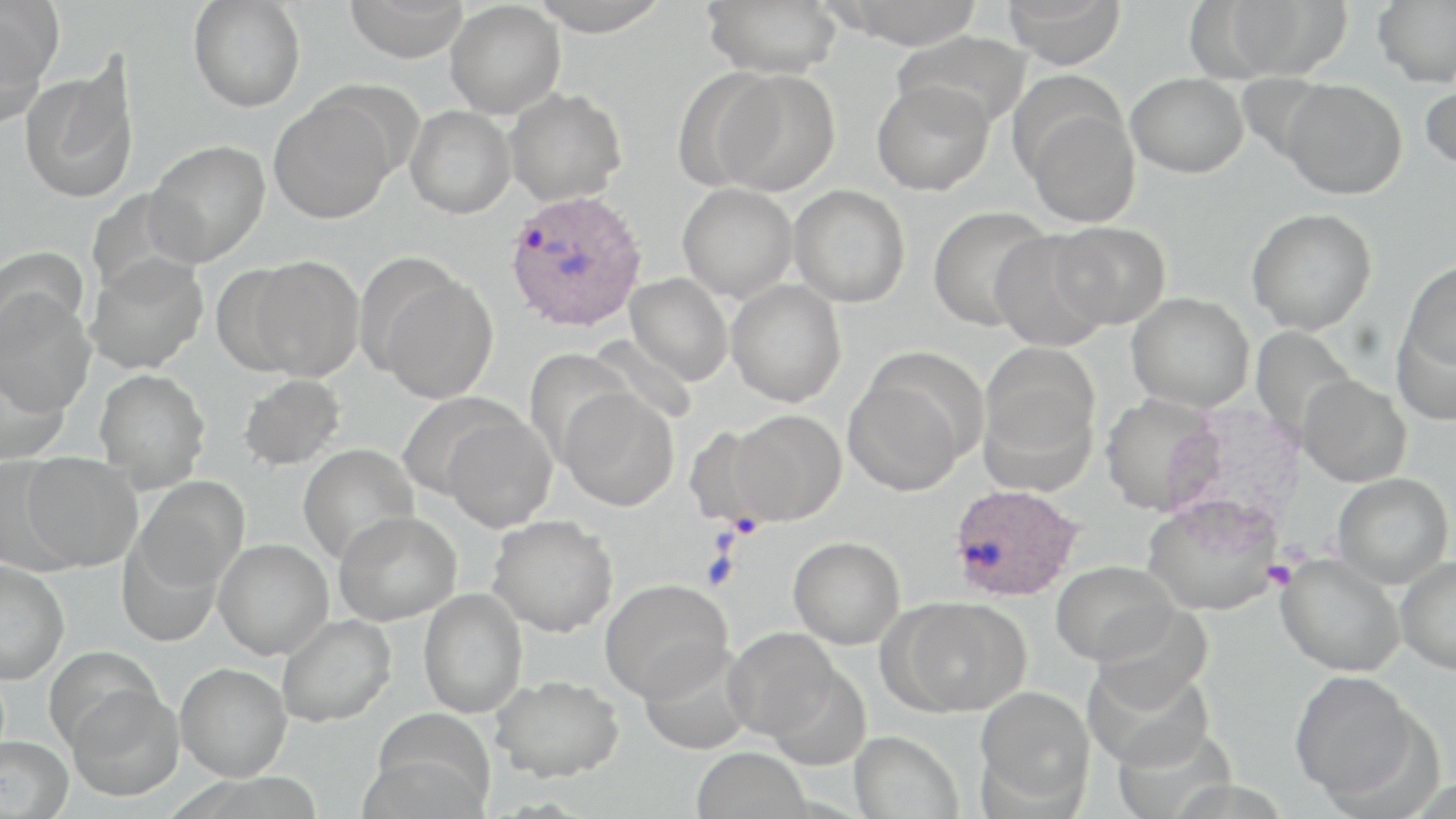
Plasmodium ovale-infected red blood cell locations = approximate bounding boxes as (x1,y1)-(x2,y2) corner pairs in pixels: (504,190)-(647,332), (948,483)-(1083,602)
slide-level diagnosis = Plasmodium ovale
field of view = one of a larger specimen
magnification = 1000x
uninfected red blood cell locations = approximate bounding boxes as (x1,y1)-(x2,y2) corner pairs in pixels: (344,0)-(471,63), (527,0)-(672,36), (831,0)-(986,50), (1001,0)-(1127,69), (1214,0)-(1351,80), (1373,0)-(1456,88), (188,1)-(306,113), (445,1)-(566,118), (701,1)-(844,78), (0,2)-(60,125), (892,29)-(1031,132), (19,65)-(139,203), (711,69)-(841,196), (1126,73)-(1248,177), (1279,78)-(1407,199), (1420,80)-(1456,174), (872,81)-(994,196), (504,88)-(627,206), (268,96)-(395,224), (1021,101)-(1141,228), (406,106)-(515,219), (145,140)-(270,266), (677,183)-(797,301), (788,184)-(910,308), (86,187)-(203,299), (927,205)-(1053,331), (1246,208)-(1377,335), (1051,221)-(1171,330), (990,230)-(1115,351), (0,247)-(88,343), (84,254)-(208,375), (242,255)-(365,381), (1399,260)-(1456,377), (373,270)-(498,404), (626,273)-(733,385), (726,280)-(847,407), (0,289)-(97,417), (1126,292)-(1254,413), (1392,309)-(1456,426), (978,341)-(1100,481), (524,347)-(636,464), (0,356)-(72,463), (94,368)-(211,492), (843,369)-(970,496), (238,374)-(346,471), (1297,374)-(1411,487), (559,388)-(679,511), (1100,393)-(1223,516), (727,409)-(846,525), (440,412)-(556,531), (298,444)-(419,564), (21,453)-(142,571), (0,455)-(80,574), (1332,472)-(1453,588), (133,475)-(250,592), (1142,494)-(1284,616), (334,510)-(462,625), (487,514)-(618,637), (116,536)-(225,645), (788,536)-(905,649), (213,538)-(333,659), (1276,553)-(1405,677), (1395,556)-(1456,675), (1051,559)-(1177,665), (0,560)-(70,683), (600,578)-(732,702), (419,588)-(528,718), (888,596)-(1032,716), (276,614)-(396,727), (723,627)-(841,742), (637,643)-(753,756), (44,645)-(162,751), (1084,658)-(1212,770), (175,662)-(292,781), (1289,667)-(1425,805), (491,674)-(623,782), (66,684)-(185,802), (975,686)-(1095,810), (363,729)-(495,819), (849,730)-(964,819), (0,735)-(73,819), (691,746)-(811,819)
image size = 1456×819 pixels
stain = May-Grünwald-Giemsa
preparation = thin blood smear
modality = optical microscopy